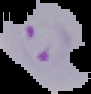 Cell region segmented out of the field of view; the surrounding area is masked to black. Image is 91×94 pixels. Malaria status: parasitized. From a thin blood smear.